Evaluate for malaria.
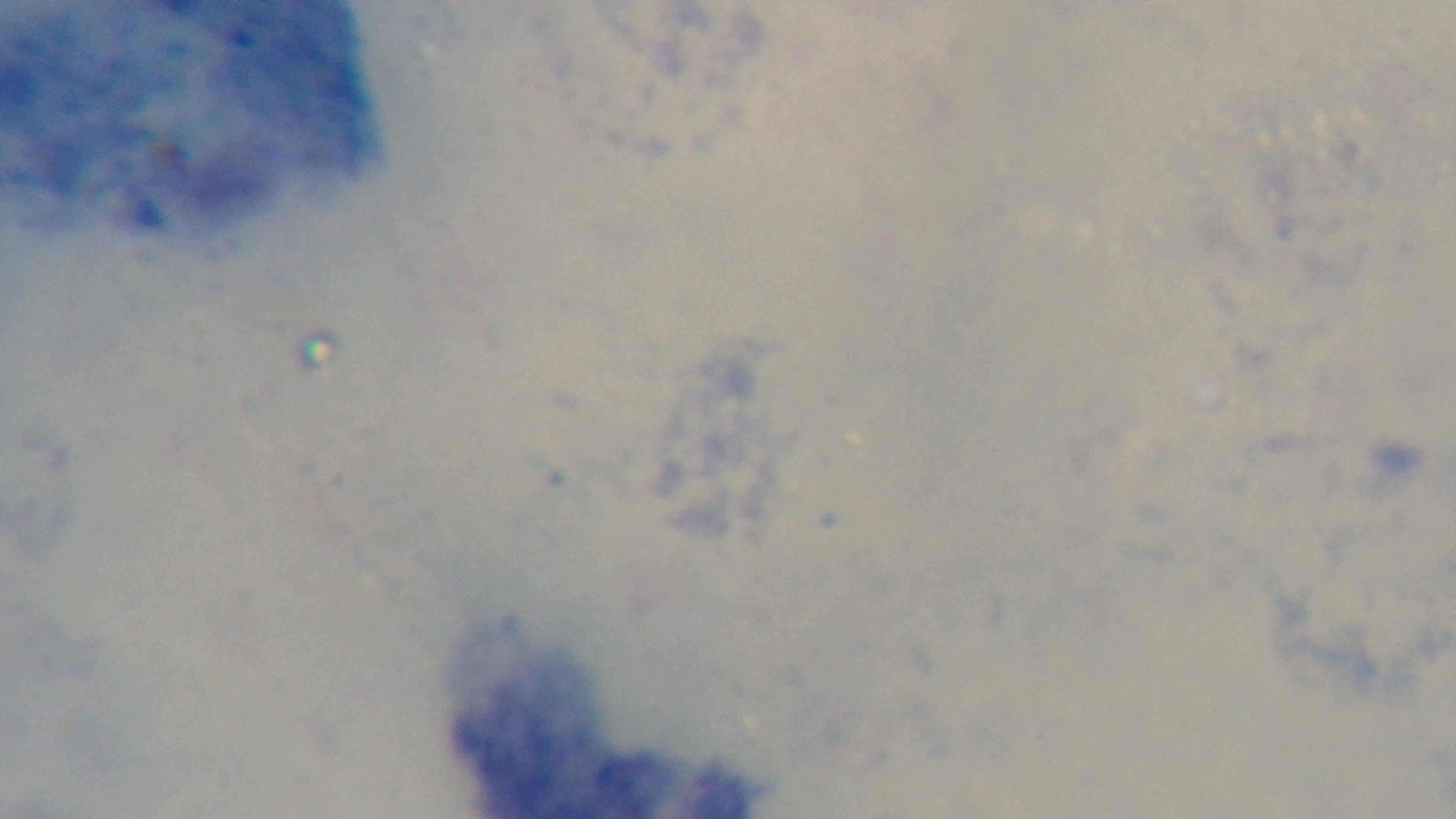
Negative.

objective = 100x oil immersion
preparation = thick blood film
field of view = single
stain = Giemsa
capture = mounted 4K digital camera
modality = light microscopy